State the blood parasite species.
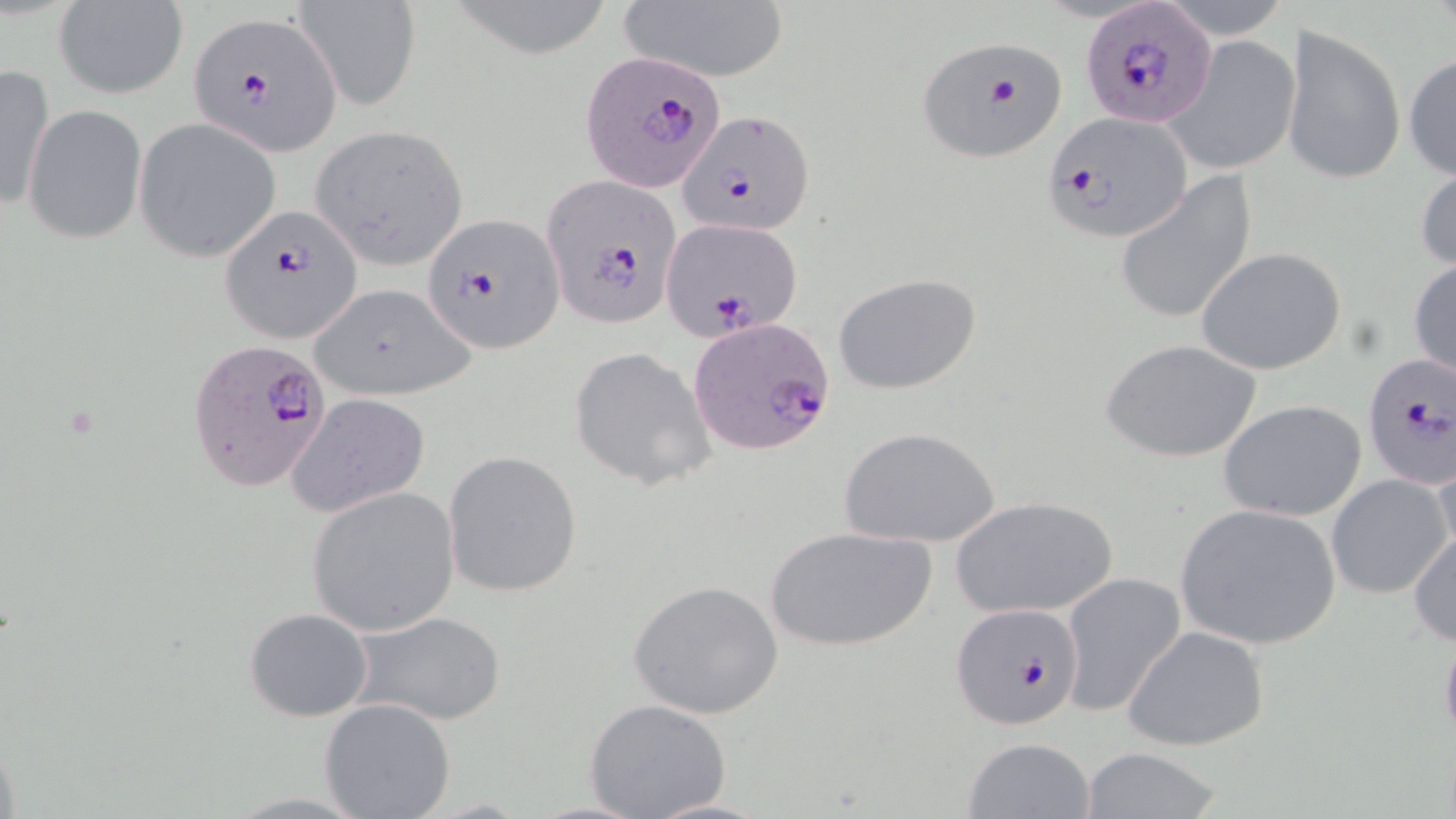

Plasmodium falciparum.

modality = light microscopy
preparation = thin blood smear
uninfected red blood cell locations = approximate bounding boxes as (x1, y1, x2, y2) in pixels: (295, 0, 421, 108), (446, 0, 615, 56), (52, 1, 188, 99), (616, 1, 790, 84), (1281, 24, 1405, 189), (1163, 34, 1300, 175), (1403, 51, 1456, 184), (0, 65, 55, 215), (21, 104, 146, 245), (134, 117, 282, 263), (308, 124, 470, 273), (1416, 156, 1456, 276), (1115, 172, 1257, 327), (1196, 246, 1350, 376), (1407, 256, 1455, 386), (833, 272, 981, 395), (309, 281, 471, 401), (1102, 338, 1262, 463), (570, 347, 715, 492), (285, 393, 432, 520), (1218, 399, 1367, 522), (839, 426, 1000, 549), (443, 450, 583, 599), (1326, 473, 1453, 598), (306, 487, 460, 637), (949, 495, 1118, 619), (1174, 504, 1342, 649), (764, 525, 936, 652), (1408, 525, 1455, 648), (1059, 571, 1185, 719), (628, 579, 783, 718), (243, 607, 373, 722), (346, 611, 508, 726), (1438, 622, 1456, 749), (1121, 625, 1270, 752), (319, 698, 456, 819), (583, 698, 731, 819), (959, 736, 1096, 819), (1077, 747, 1224, 819), (641, 796, 778, 818)
image size = 1456×819 pixels
stain = May-Grünwald-Giemsa
Plasmodium falciparum-infected red blood cell locations = approximate bounding boxes as (x1, y1, x2, y2) in pixels: (1081, 3, 1216, 128), (187, 10, 343, 154), (915, 37, 1068, 162), (582, 49, 728, 193), (678, 109, 813, 238), (1044, 111, 1194, 242), (540, 173, 682, 330), (218, 203, 362, 343), (423, 213, 562, 353), (661, 217, 803, 343), (689, 318, 837, 456), (187, 338, 334, 493), (1361, 355, 1454, 489), (951, 602, 1085, 730)
magnification = 1000x
field of view = single